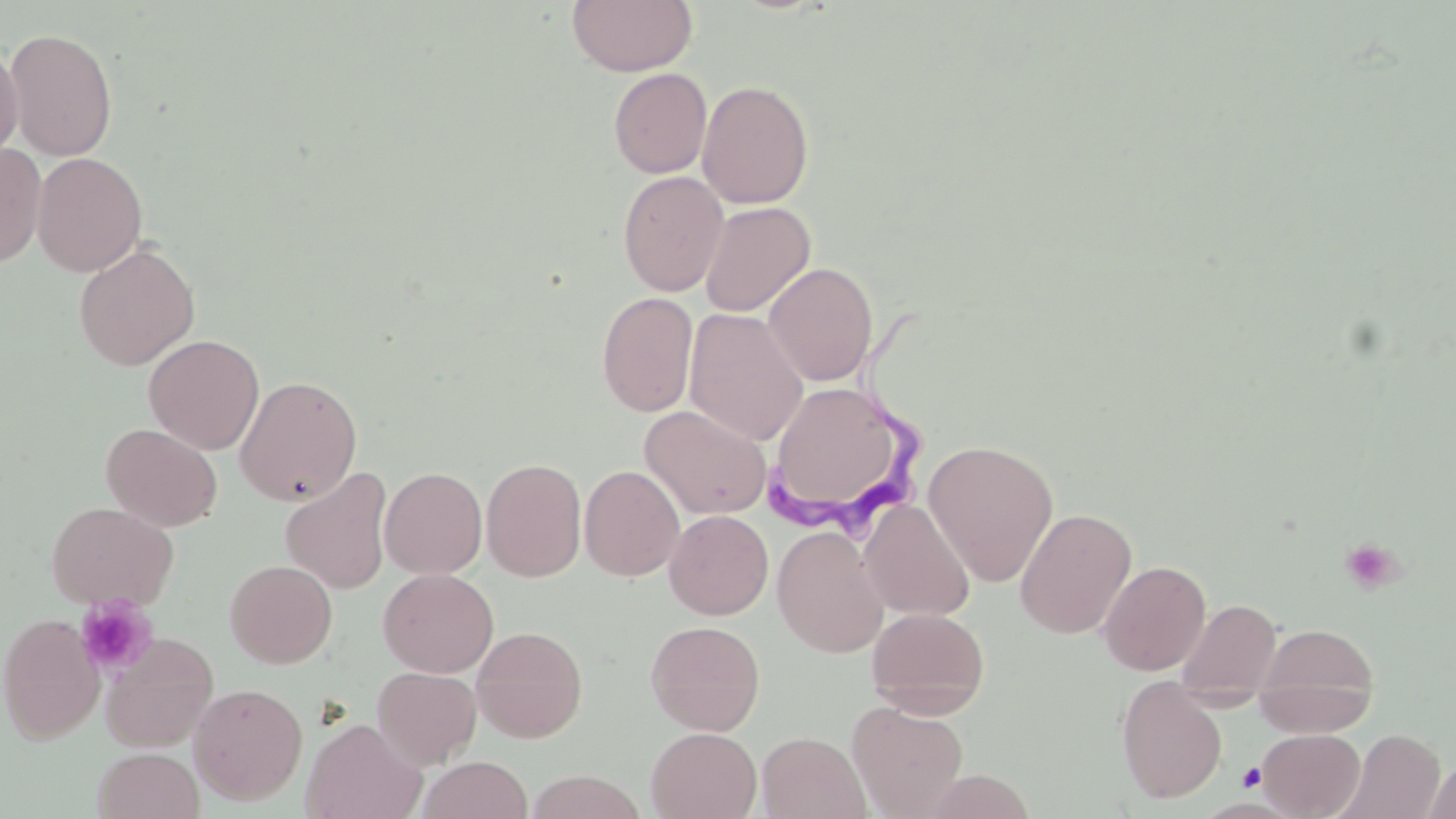

Summary:
  - Coordinate format: approximate bounding boxes as (x1,y1)-(x2,y2) corner pairs in pixels
  - Trypanosoma brucei locations: (763,297)-(934,526)
  - Uninfected red blood cell locations: (566,0)-(698,76), (4,27)-(118,162), (0,42)-(23,163), (608,67)-(712,178), (696,80)-(815,209), (0,143)-(46,269), (32,152)-(147,277), (617,171)-(728,296), (698,201)-(815,317), (73,243)-(200,371), (763,261)-(878,386), (596,291)-(698,417), (684,308)-(808,446), (143,334)-(264,454), (234,375)-(363,506), (772,392)-(900,502), (639,405)-(772,519), (101,423)-(222,532), (923,439)-(1059,586), (480,457)-(587,582), (579,464)-(686,581), (281,467)-(393,595), (379,467)-(488,578), (859,499)-(975,621), (45,500)-(178,612), (1015,507)-(1137,638), (664,510)-(774,620), (663,515)-(890,630), (771,525)-(890,657), (1098,559)-(1211,676), (225,560)-(338,668), (378,567)-(499,677), (1176,599)-(1282,699), (866,607)-(988,718), (1,613)-(104,744), (645,620)-(765,736), (1254,622)-(1380,731), (471,625)-(588,742), (100,632)-(218,752), (372,666)-(482,768), (1116,677)-(1227,803), (190,682)-(308,805), (847,700)-(969,818), (301,718)-(426,819), (646,727)-(762,818), (1258,728)-(1365,818), (1335,728)-(1445,819), (756,732)-(871,818), (93,748)-(204,819), (417,756)-(534,819), (1424,760)-(1456,819)
  - Platelet locations: (1338,536)-(1405,596), (75,595)-(158,679), (1237,763)-(1265,791)
  - Slide-level diagnosis: Trypanosoma brucei
  - Modality: optical microscopy
  - Preparation: thin blood film
  - Stain: May-Grünwald-Giemsa
  - Field of view: one of a larger specimen
  - Magnification: 1000x
  - Image size: 1456×819 pixels